Locate and identify every blood parasite.
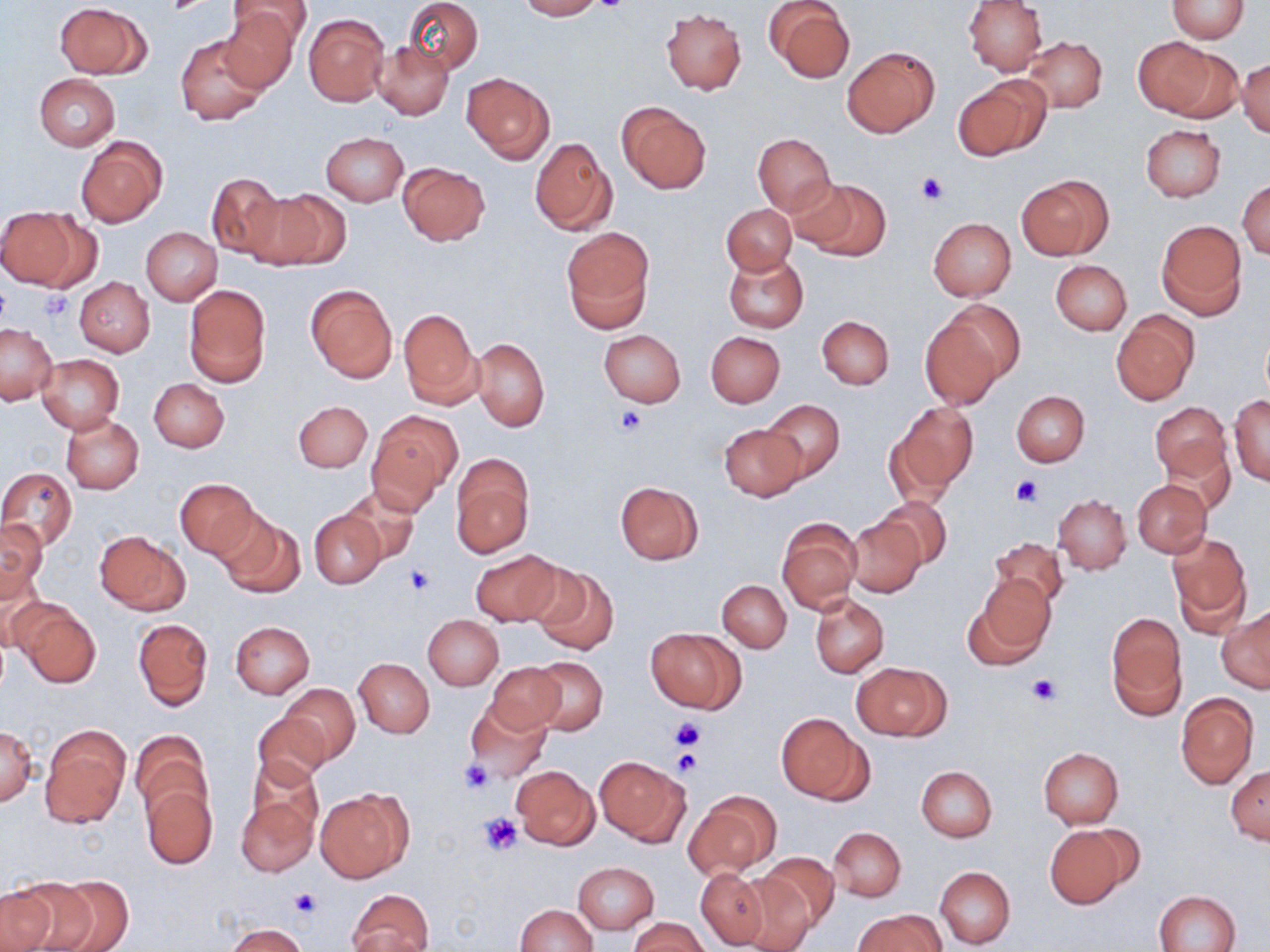
No blood parasites observed.

Summary:
  - Coordinate format: approximate bounding boxes as named x1/y1/x2/y2 corners in pixels
  - Uninfected red blood cell locations: (x1=404, y1=0, x2=483, y2=74), (x1=515, y1=0, x2=605, y2=20), (x1=962, y1=0, x2=1047, y2=75), (x1=1167, y1=0, x2=1249, y2=41), (x1=224, y1=1, x2=310, y2=52), (x1=54, y1=2, x2=150, y2=79), (x1=763, y1=2, x2=856, y2=84), (x1=217, y1=5, x2=302, y2=92), (x1=660, y1=9, x2=746, y2=95), (x1=304, y1=13, x2=389, y2=107), (x1=177, y1=35, x2=268, y2=126), (x1=1021, y1=36, x2=1108, y2=113), (x1=1137, y1=38, x2=1240, y2=120), (x1=373, y1=41, x2=454, y2=120), (x1=842, y1=47, x2=940, y2=137), (x1=1237, y1=57, x2=1270, y2=138), (x1=461, y1=72, x2=555, y2=164), (x1=34, y1=73, x2=121, y2=150), (x1=953, y1=76, x2=1050, y2=161), (x1=616, y1=102, x2=711, y2=195), (x1=1140, y1=124, x2=1226, y2=201), (x1=320, y1=131, x2=409, y2=205), (x1=752, y1=133, x2=835, y2=215), (x1=75, y1=136, x2=167, y2=226), (x1=530, y1=137, x2=615, y2=237), (x1=398, y1=161, x2=490, y2=246), (x1=205, y1=172, x2=287, y2=261), (x1=1016, y1=174, x2=1113, y2=261), (x1=796, y1=178, x2=890, y2=261), (x1=1238, y1=180, x2=1270, y2=259), (x1=247, y1=187, x2=351, y2=271), (x1=722, y1=204, x2=796, y2=275), (x1=0, y1=207, x2=82, y2=290), (x1=928, y1=217, x2=1016, y2=300), (x1=1157, y1=219, x2=1247, y2=317), (x1=141, y1=227, x2=222, y2=305), (x1=561, y1=227, x2=654, y2=332), (x1=722, y1=251, x2=809, y2=334), (x1=1050, y1=260, x2=1132, y2=335), (x1=75, y1=277, x2=155, y2=356), (x1=305, y1=284, x2=397, y2=382), (x1=184, y1=285, x2=271, y2=387), (x1=940, y1=299, x2=1027, y2=384), (x1=399, y1=308, x2=482, y2=409), (x1=1112, y1=311, x2=1199, y2=406), (x1=816, y1=316, x2=894, y2=389), (x1=920, y1=319, x2=1003, y2=409), (x1=0, y1=324, x2=56, y2=404), (x1=598, y1=329, x2=686, y2=407), (x1=705, y1=332, x2=785, y2=408), (x1=471, y1=336, x2=549, y2=431), (x1=36, y1=354, x2=125, y2=432), (x1=149, y1=379, x2=230, y2=452), (x1=1012, y1=390, x2=1089, y2=467), (x1=1229, y1=395, x2=1270, y2=484), (x1=760, y1=399, x2=845, y2=483), (x1=293, y1=400, x2=373, y2=473), (x1=1151, y1=402, x2=1231, y2=483), (x1=895, y1=403, x2=977, y2=493), (x1=367, y1=412, x2=461, y2=509), (x1=60, y1=413, x2=144, y2=494), (x1=719, y1=424, x2=804, y2=501), (x1=1161, y1=437, x2=1235, y2=511), (x1=450, y1=455, x2=534, y2=557), (x1=0, y1=467, x2=77, y2=550), (x1=174, y1=477, x2=260, y2=560), (x1=1133, y1=480, x2=1212, y2=557), (x1=614, y1=481, x2=705, y2=565), (x1=341, y1=485, x2=421, y2=566), (x1=1052, y1=495, x2=1130, y2=574), (x1=875, y1=496, x2=953, y2=569), (x1=215, y1=510, x2=306, y2=599), (x1=310, y1=510, x2=385, y2=588), (x1=1, y1=518, x2=47, y2=597), (x1=847, y1=518, x2=924, y2=597), (x1=778, y1=519, x2=861, y2=614), (x1=95, y1=530, x2=188, y2=613), (x1=1168, y1=533, x2=1250, y2=626), (x1=988, y1=536, x2=1070, y2=610), (x1=469, y1=549, x2=567, y2=626), (x1=0, y1=564, x2=50, y2=652), (x1=530, y1=564, x2=619, y2=655), (x1=971, y1=575, x2=1056, y2=663), (x1=718, y1=580, x2=791, y2=652), (x1=811, y1=594, x2=889, y2=677), (x1=14, y1=601, x2=103, y2=686), (x1=1219, y1=609, x2=1270, y2=693), (x1=423, y1=615, x2=503, y2=690), (x1=1106, y1=615, x2=1188, y2=719), (x1=133, y1=618, x2=213, y2=710), (x1=231, y1=621, x2=314, y2=697), (x1=646, y1=628, x2=745, y2=713), (x1=354, y1=658, x2=435, y2=737), (x1=528, y1=658, x2=608, y2=734), (x1=854, y1=662, x2=949, y2=740), (x1=486, y1=663, x2=569, y2=734), (x1=281, y1=684, x2=360, y2=766), (x1=1175, y1=693, x2=1258, y2=788), (x1=464, y1=699, x2=551, y2=781), (x1=251, y1=711, x2=330, y2=790), (x1=775, y1=712, x2=869, y2=803), (x1=39, y1=725, x2=130, y2=828), (x1=0, y1=726, x2=38, y2=806), (x1=131, y1=730, x2=213, y2=823), (x1=1039, y1=748, x2=1124, y2=827), (x1=595, y1=755, x2=690, y2=844), (x1=247, y1=760, x2=323, y2=844), (x1=512, y1=765, x2=599, y2=849), (x1=1226, y1=765, x2=1270, y2=842), (x1=917, y1=766, x2=997, y2=841), (x1=141, y1=784, x2=216, y2=868), (x1=316, y1=787, x2=413, y2=882), (x1=685, y1=790, x2=779, y2=880), (x1=235, y1=792, x2=320, y2=878), (x1=1044, y1=823, x2=1135, y2=907), (x1=828, y1=826, x2=907, y2=901), (x1=753, y1=851, x2=839, y2=934), (x1=573, y1=862, x2=659, y2=935), (x1=935, y1=867, x2=1015, y2=949), (x1=695, y1=869, x2=769, y2=949), (x1=733, y1=871, x2=820, y2=952), (x1=47, y1=877, x2=133, y2=952), (x1=11, y1=878, x2=98, y2=952), (x1=0, y1=887, x2=57, y2=952), (x1=346, y1=888, x2=435, y2=952), (x1=1154, y1=890, x2=1241, y2=952), (x1=514, y1=904, x2=598, y2=952), (x1=854, y1=910, x2=944, y2=952), (x1=628, y1=916, x2=711, y2=952), (x1=226, y1=923, x2=309, y2=951)
  - Platelet locations: (x1=590, y1=0, x2=629, y2=15), (x1=917, y1=172, x2=948, y2=204), (x1=40, y1=289, x2=74, y2=321), (x1=614, y1=407, x2=647, y2=436), (x1=1012, y1=477, x2=1042, y2=507), (x1=403, y1=565, x2=434, y2=596), (x1=1027, y1=674, x2=1061, y2=706), (x1=671, y1=715, x2=704, y2=751), (x1=672, y1=749, x2=700, y2=777), (x1=457, y1=759, x2=497, y2=795), (x1=480, y1=813, x2=525, y2=854), (x1=289, y1=886, x2=320, y2=920)
  - Slide-level diagnosis: no evidence of blood parasites
  - Field of view: single
  - Modality: optical microscopy
  - Image size: 1270×952 pixels
  - Magnification: 1000x
  - Preparation: thin blood smear
  - Stain: May-Grünwald-Giemsa